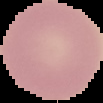

Summary:
  - Malaria status: uninfected
  - Image type: segmented cell region on a black background
  - Image size: 103×103 pixels
  - Preparation: thin blood film